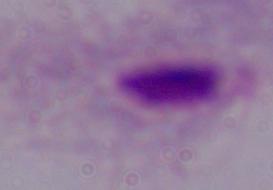
Micrograph. 1000x magnification. A trichomonad is shown.